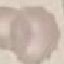

result: no malaria parasites detected
preparation: thin blood film
capture: smartphone camera at the microscope eyepiece
stain: Giemsa
image_type: cell patch, automatically extracted from a larger field of view and resized to 64 × 64 pixels